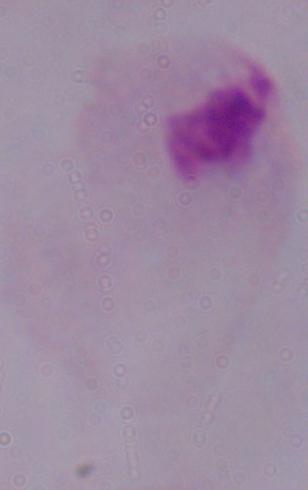

A trichomonad is seen. Micrograph. Captured at 1000x magnification.